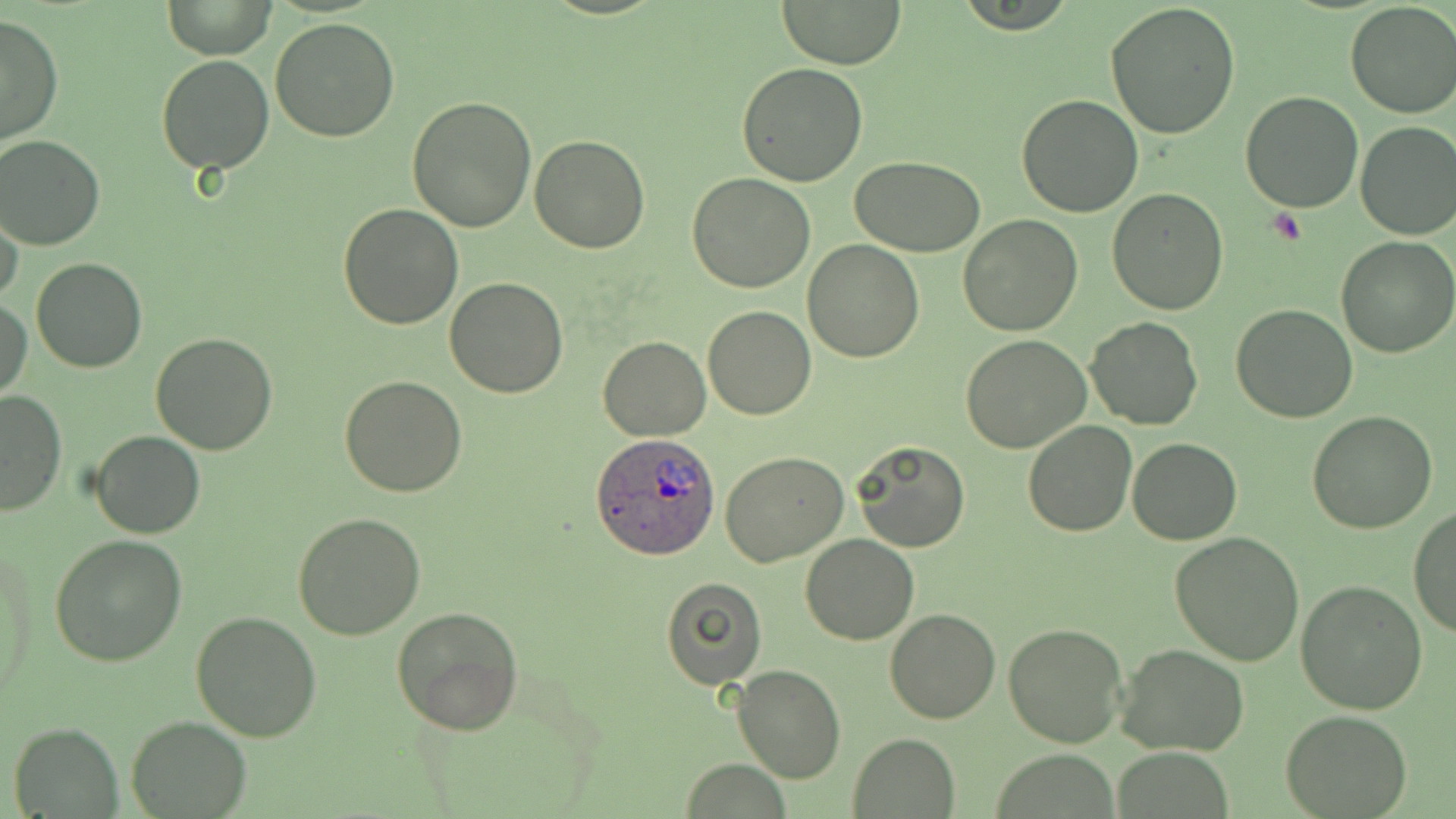
Approximate bounding boxes as (x1,y1)-(x2,y2) corner pairs in pixels. Plasmodium ovale-infected red blood cell locations: (593,432)-(721,559). Uninfected red blood cell locations: (164,0)-(276,58), (779,0)-(906,69), (1344,1)-(1456,120), (1106,2)-(1241,139), (0,15)-(63,145), (269,15)-(401,142), (155,54)-(274,174), (737,62)-(869,187), (1240,90)-(1364,212), (1015,94)-(1143,217), (405,96)-(537,231), (1354,120)-(1456,239), (0,135)-(104,251), (530,136)-(651,255), (851,156)-(987,255), (687,172)-(816,293), (1107,188)-(1230,314), (337,203)-(464,331), (0,206)-(25,308), (957,215)-(1083,336), (1335,235)-(1456,358), (802,239)-(924,363), (30,256)-(147,373), (443,277)-(569,399), (0,298)-(32,400), (1231,303)-(1359,423), (703,305)-(816,420), (1084,316)-(1202,429), (150,333)-(279,455), (960,335)-(1092,454), (597,336)-(710,439), (339,375)-(468,497), (0,390)-(66,516), (1306,410)-(1438,534), (1022,420)-(1138,537), (90,429)-(204,540), (1127,437)-(1242,546), (851,440)-(970,553), (721,452)-(848,568), (1409,507)-(1456,638), (292,514)-(426,641), (1169,532)-(1305,666), (50,534)-(187,665), (800,534)-(918,645), (2,540)-(38,692), (660,577)-(767,689), (1297,581)-(1428,716), (392,605)-(524,735), (883,609)-(1000,725), (191,610)-(323,741), (1003,624)-(1129,748), (1116,644)-(1250,757), (731,664)-(846,783), (1281,710)-(1411,818), (126,715)-(251,817), (9,723)-(122,816), (847,734)-(961,817), (1115,747)-(1234,819), (679,760)-(794,817). Platelet locations: (1270,207)-(1308,246). Slide-level diagnosis: Plasmodium ovale. Thin blood film. Captured at 1000x magnification. Light microscopy. Single field of view. Image is 1456×819 pixels. May-Grünwald-Giemsa stain.